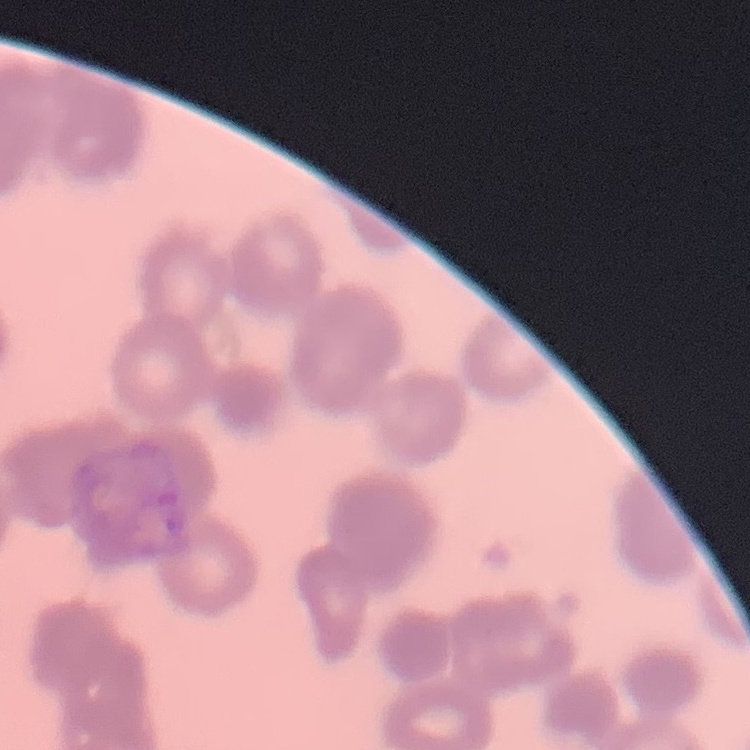

The erythrocytes exhibit rouleaux formation. Square crop of a larger photomicrograph. Thin blood smear. Field's or Giemsa stain.